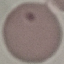 Result: no malaria parasites seen. Acquired by smartphone through the microscope eyepiece. Giemsa stain. Automatically extracted cell patch, resized to 64 × 64 pixels. Thin blood film.